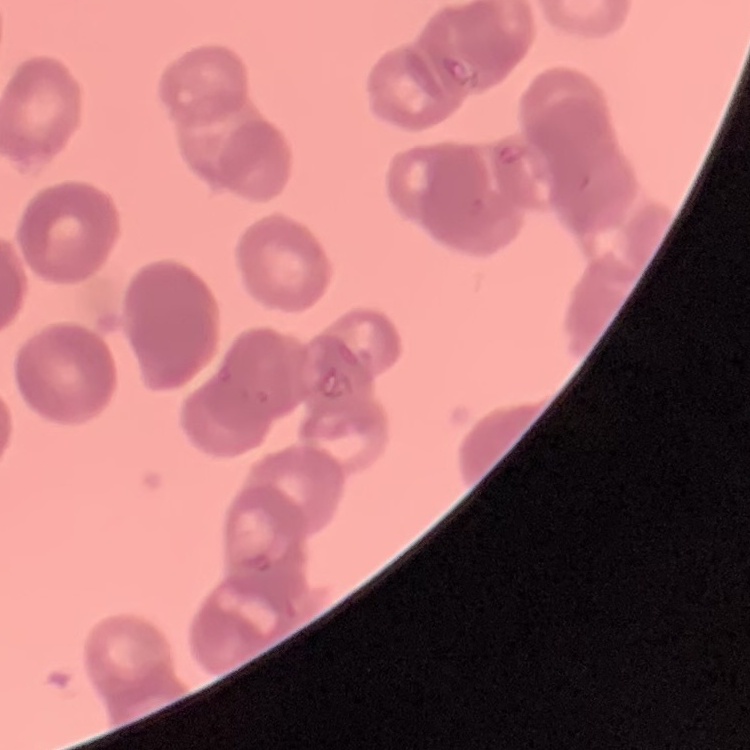
The erythrocytes show rouleaux formation. Thin blood film. One tile cut from a larger photomicrograph. Field's or Giemsa stain.